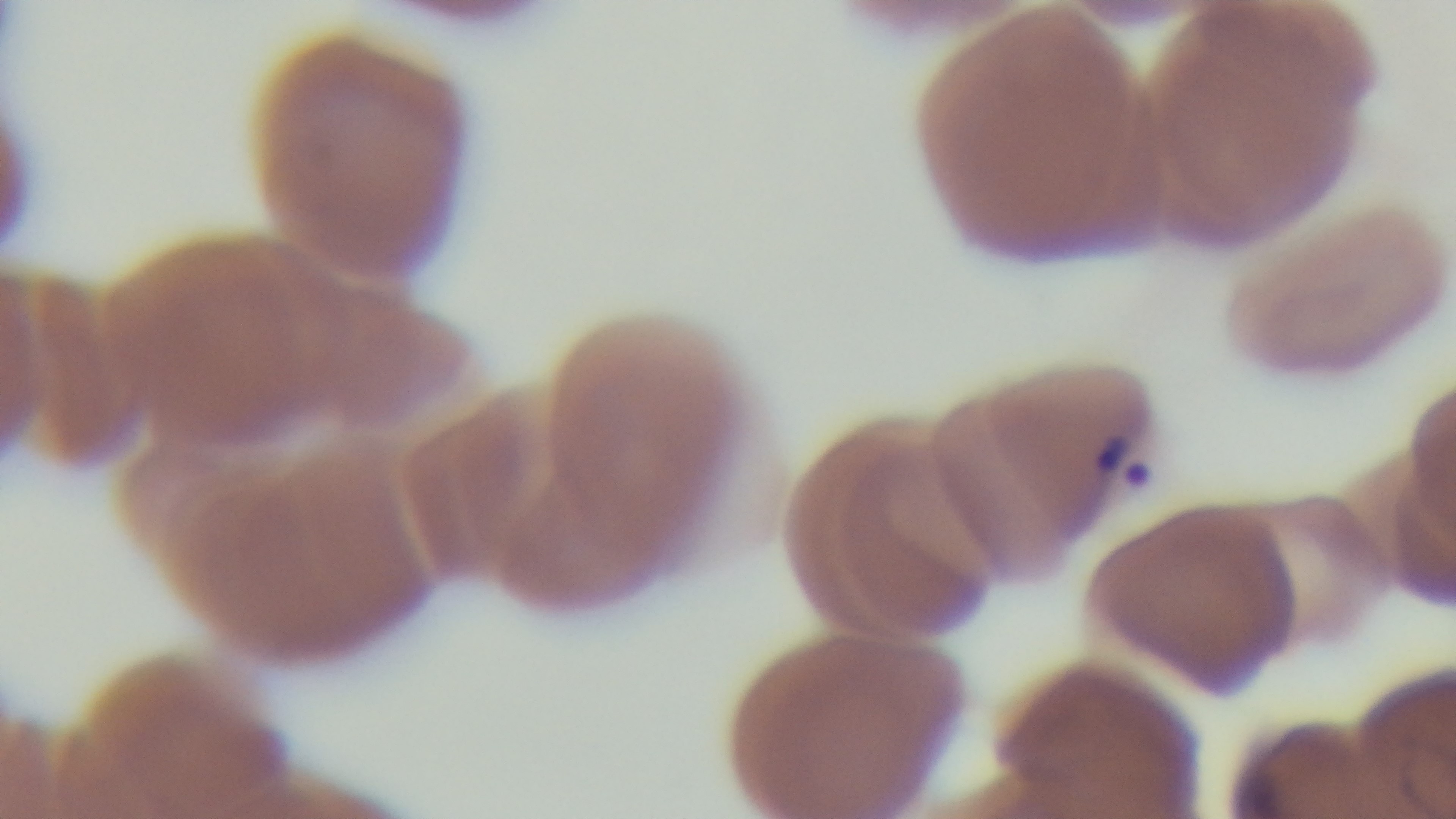
Preparation: thin. Single field of view. Oil-immersion objective, 100x. Mounted 4K digital camera. Giemsa-stained. Malaria status: infected. Light microscopy.